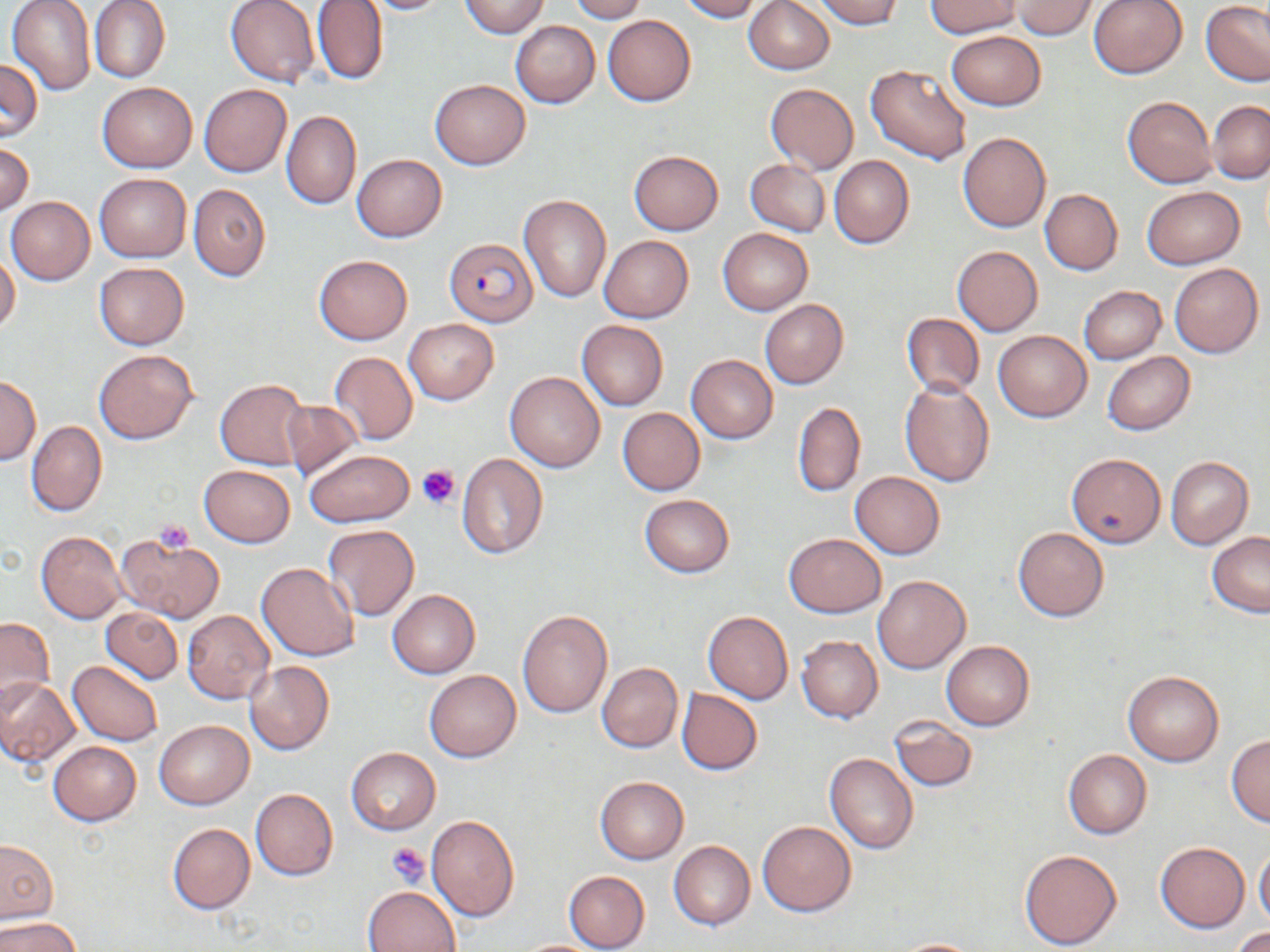 Approximate bounding boxes as (x1,y1)-(x2,y2) corner pairs in pixels. Uninfected red blood cell locations: (7,0)-(96,97), (89,0)-(170,83), (224,0)-(320,86), (356,0)-(454,14), (568,0)-(646,22), (677,0)-(763,21), (814,0)-(906,30), (924,0)-(1022,37), (1013,0)-(1098,39), (1088,0)-(1187,79), (312,1)-(387,87), (459,1)-(549,37), (743,1)-(834,74), (1201,3)-(1270,85), (602,16)-(695,106), (510,20)-(600,107), (946,31)-(1045,110), (0,59)-(42,142), (865,63)-(972,166), (430,79)-(530,168), (97,82)-(197,172), (765,83)-(858,174), (199,84)-(292,178), (1122,95)-(1216,187), (1207,100)-(1270,183), (281,110)-(361,209), (958,132)-(1051,232), (0,141)-(33,217), (629,150)-(723,234), (352,154)-(446,242), (829,155)-(913,249), (744,158)-(830,238), (94,173)-(191,262), (188,184)-(270,282), (1141,186)-(1244,268), (1039,189)-(1123,275), (517,194)-(612,302), (5,196)-(94,284), (717,229)-(812,315), (598,235)-(692,323), (952,246)-(1042,336), (314,254)-(412,344), (0,256)-(19,334), (94,262)-(189,349), (1169,263)-(1263,358), (1078,285)-(1166,363), (759,300)-(848,389), (900,313)-(984,397), (403,319)-(498,404), (577,320)-(667,410), (992,330)-(1091,421), (94,349)-(198,444), (1102,351)-(1194,435), (328,352)-(418,445), (687,355)-(777,443), (504,371)-(605,472), (1,377)-(40,464), (215,379)-(310,470), (900,381)-(994,486), (280,400)-(360,480), (793,401)-(866,498), (617,407)-(705,495), (25,421)-(106,517), (303,449)-(414,526), (456,453)-(549,558), (1066,453)-(1166,549), (1165,457)-(1254,548), (198,465)-(294,547), (850,471)-(945,558), (639,494)-(734,577), (323,525)-(419,620), (1013,527)-(1108,621), (37,531)-(126,622), (115,533)-(224,625), (783,533)-(884,617), (1207,533)-(1270,617), (256,562)-(359,661), (871,574)-(971,673), (388,590)-(480,678), (101,608)-(182,684), (517,609)-(612,717), (183,610)-(273,703), (703,610)-(793,704), (0,616)-(54,713), (796,635)-(883,723), (941,641)-(1033,730), (67,660)-(162,745), (244,661)-(334,756), (596,662)-(682,753), (424,670)-(521,761), (1123,670)-(1224,766), (0,678)-(80,769), (676,688)-(762,775), (889,714)-(978,792), (155,720)-(253,809), (1226,735)-(1270,827), (48,741)-(141,825), (346,748)-(440,834), (1063,749)-(1152,839), (824,752)-(918,854), (594,776)-(688,864), (249,787)-(337,880), (426,815)-(520,921), (756,820)-(856,916), (167,823)-(254,914), (0,840)-(57,923), (669,841)-(755,929), (1155,843)-(1249,932), (1019,848)-(1122,950), (1255,848)-(1270,930), (563,871)-(650,952), (363,886)-(460,951), (0,916)-(82,952), (1231,928)-(1270,951), (888,938)-(988,951), (512,939)-(607,951). Platelet locations: (416,463)-(462,509), (152,520)-(194,555), (387,842)-(432,887). Plasmodium falciparum-infected red blood cell locations: (446,238)-(537,326). Slide-level diagnosis: Plasmodium falciparum. One field of a larger specimen. Thin blood smear. Image is 1270×952 pixels. Light microscopy. May-Grünwald-Giemsa-stained preparation. Captured at 1000x magnification.